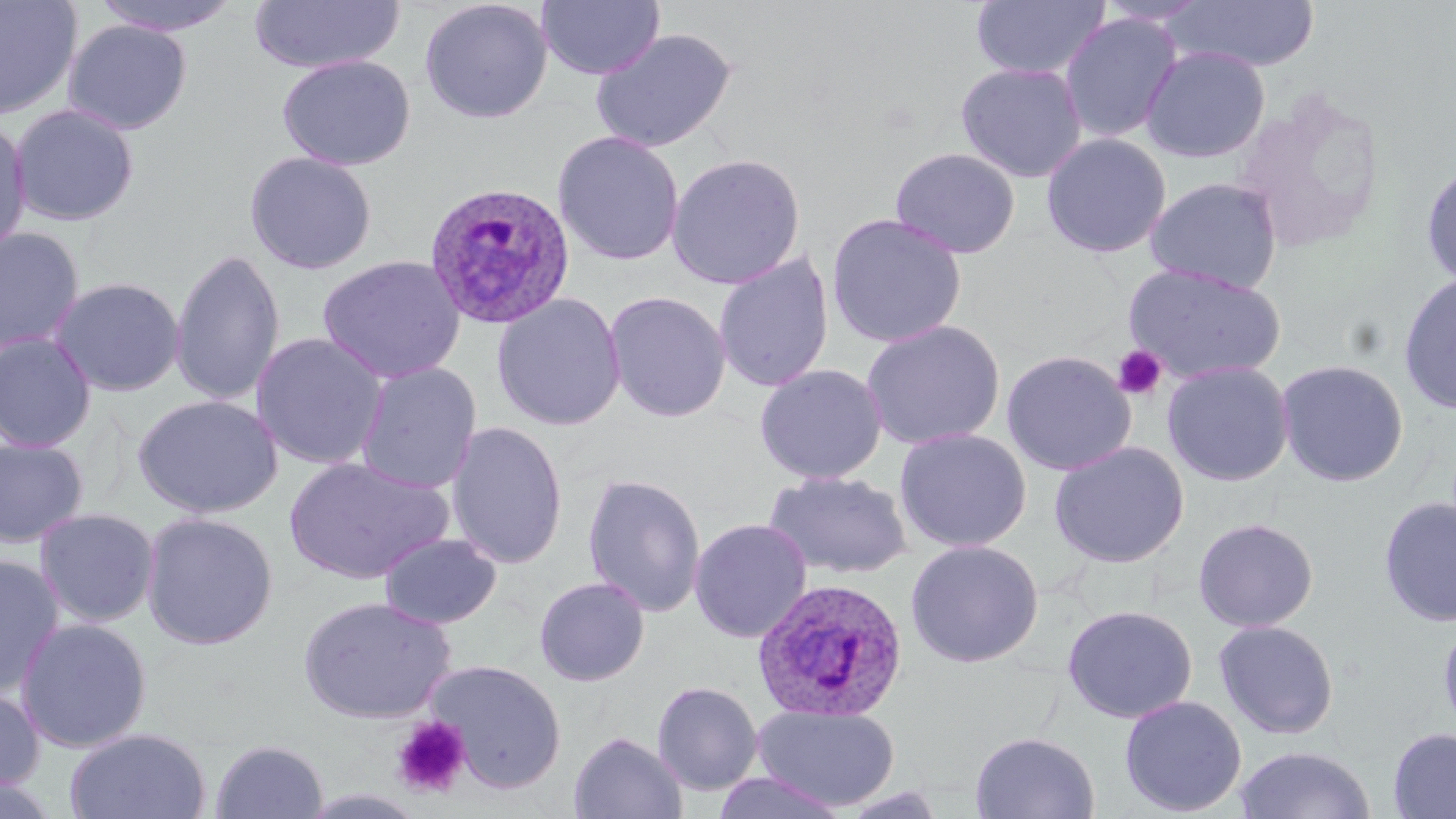 Approximate bounding boxes as (x1,y1)-(x2,y2) corner pairs in pixels. Platelet locations: (1111,344)-(1167,402), (391,716)-(471,798). Uninfected red blood cell locations: (0,0)-(83,121), (90,0)-(244,37), (419,0)-(554,124), (537,0)-(664,82), (969,0)-(1111,81), (1095,0)-(1211,27), (1165,0)-(1320,73), (247,1)-(404,74), (1059,12)-(1184,144), (62,19)-(193,136), (590,27)-(737,154), (1141,46)-(1270,164), (276,54)-(415,171), (955,61)-(1087,183), (1232,89)-(1387,255), (9,103)-(140,227), (0,115)-(32,261), (552,130)-(685,266), (1040,132)-(1172,259), (889,147)-(1021,259), (243,150)-(378,275), (666,152)-(806,290), (1420,159)-(1456,290), (1144,176)-(1282,294), (826,212)-(967,348), (0,226)-(85,357), (170,247)-(286,407), (713,250)-(835,393), (317,254)-(466,384), (1122,262)-(1286,384), (1398,271)-(1456,415), (50,276)-(185,397), (603,290)-(732,423), (491,292)-(627,431), (860,319)-(1006,451), (0,331)-(98,452), (251,332)-(389,471), (1001,350)-(1137,477), (1275,358)-(1410,487), (1161,360)-(1295,487), (354,362)-(483,494), (753,363)-(888,485), (132,393)-(284,519), (446,420)-(569,570), (894,427)-(1032,553), (0,437)-(89,548), (1049,440)-(1190,568), (283,456)-(453,584), (763,470)-(915,580), (582,472)-(706,618), (1378,495)-(1456,628), (35,507)-(160,628), (141,511)-(279,650), (1192,517)-(1319,633), (688,518)-(813,643), (379,532)-(502,629), (905,539)-(1044,668), (0,554)-(65,699), (533,576)-(650,687), (297,594)-(456,724), (1061,604)-(1198,724), (1437,612)-(1456,741), (15,617)-(153,752), (1213,620)-(1340,739), (424,658)-(568,793), (651,680)-(764,796), (0,683)-(45,795), (1118,695)-(1248,816), (751,704)-(900,811), (65,727)-(212,819), (1387,727)-(1456,819), (568,731)-(688,818), (969,731)-(1101,818), (210,739)-(329,819), (1233,745)-(1376,819), (710,770)-(851,818), (0,775)-(64,819). Plasmodium ovale-infected red blood cell locations: (423,180)-(577,330), (751,577)-(910,722). Slide-level diagnosis: Plasmodium ovale. 1000x magnification. Thin blood smear. One field of a larger specimen. Image is 1456×819 pixels. May-Grünwald-Giemsa-stained preparation. Light microscopy.